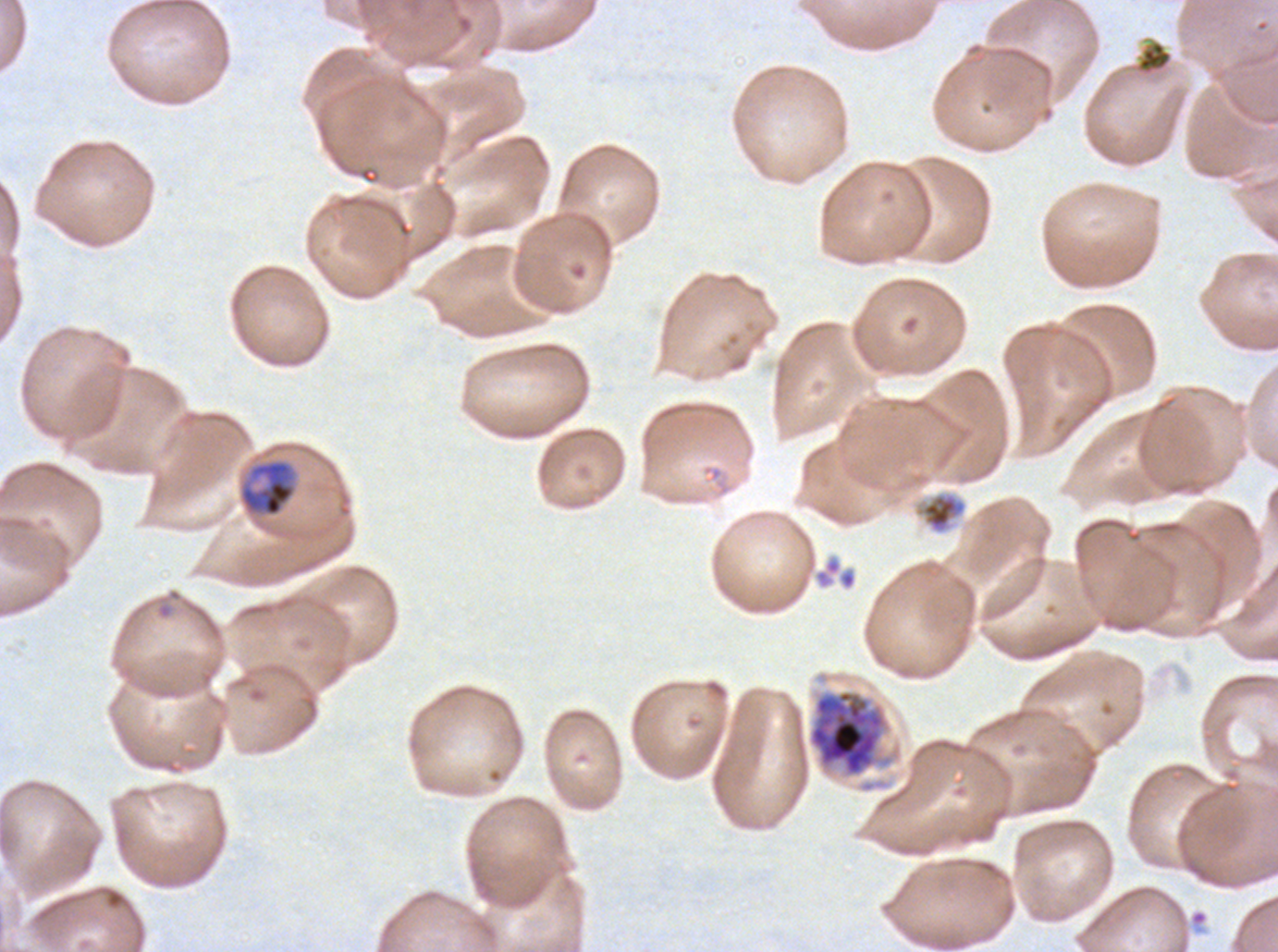

specimen: Plasmodium falciparum cultured ex vivo for 24 to 48 hours, from a patient in The Gambia
preparation: thin blood film
debris_locations: 'approximate bounding boxes as (x1, y1, x2, y2) in pixels: (1135, 39, 1174, 76), (914, 491, 967, 534), (813, 555, 857, 591)'
mid_trophozoite_locations: 'approximate bounding boxes as (x1, y1, x2, y2) in pixels: (238, 458, 298, 518)'
life_cycle_stages_observed: mid trophozoite, early schizont
image_size: 1278×952 pixels
field_of_view: one sub-image of a larger composite
stain: Giemsa
early_schizont_locations: 'approximate bounding boxes as (x1, y1, x2, y2) in pixels: (808, 690, 886, 776)'